Assess this cell for malaria.
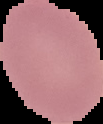

Uninfected.

Image is 103×124 pixels. From a thin blood smear. The area outside the segmented cell region is set to black.